Evaluate for malaria.
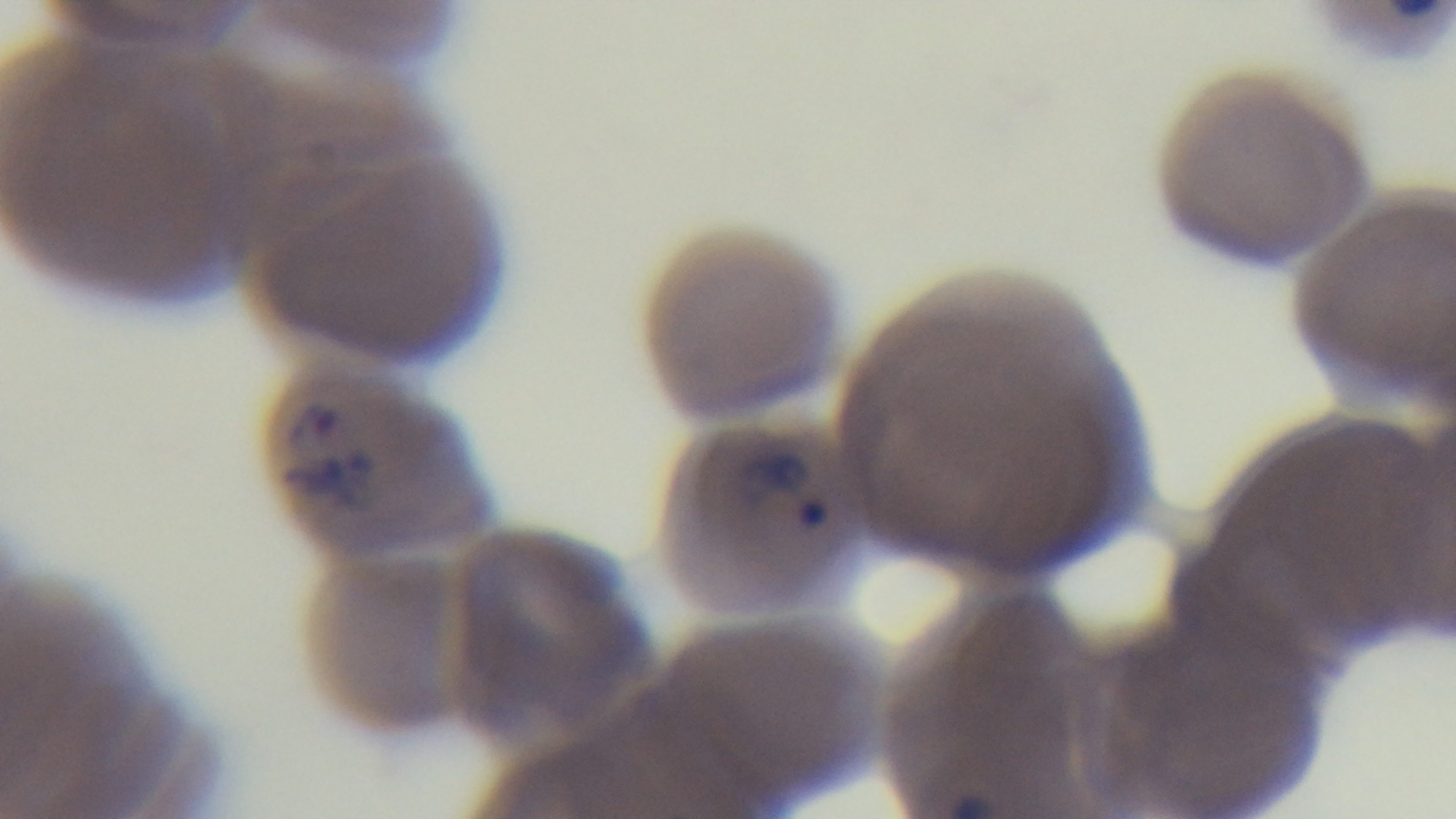
Infected.

{
  "modality": "light microscopy",
  "stain": "Giemsa",
  "capture": "mounted 4K digital camera",
  "field_of_view": "one from the slide",
  "preparation": "thin",
  "objective": "100x oil immersion"
}